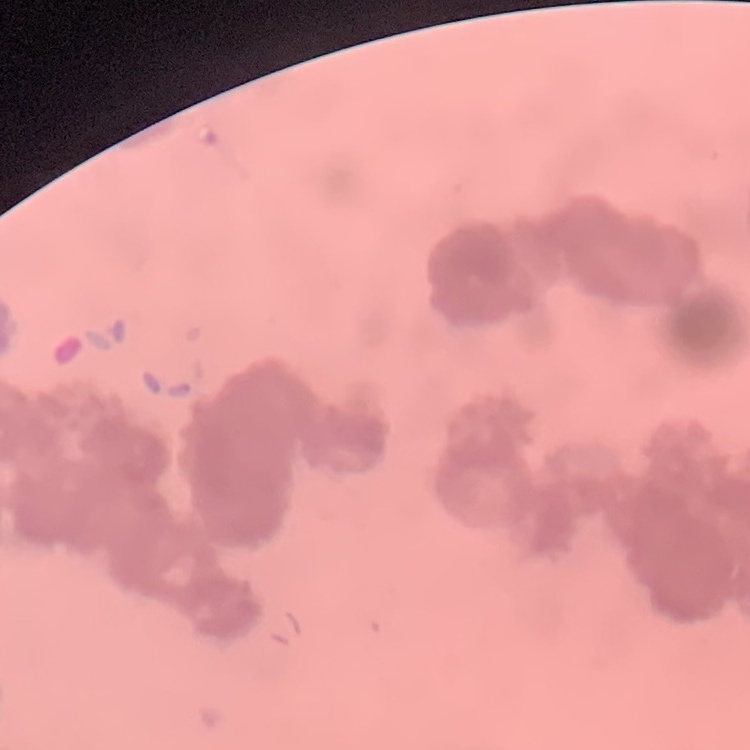
erythrocyte morphology = rouleaux formation
stain = Field's or Giemsa
image type = one tile cut from a larger photomicrograph
preparation = thin peripheral smear